Report the malaria status of this cell.
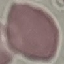

It is uninfected.

image_type: cell patch, automatically extracted from a larger field of view and resized to 64 × 64 pixels
preparation: thin blood film
capture: smartphone camera at the microscope eyepiece
stain: Giemsa